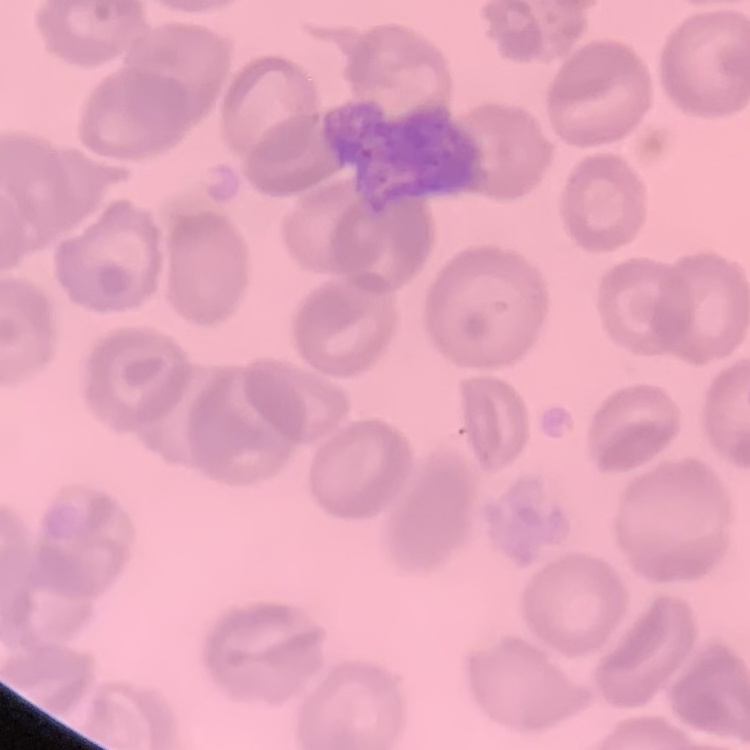

The red blood cells exhibit no rouleaux formation. One tile cut from a larger photomicrograph. Thin peripheral smear. Field's or Giemsa stain.